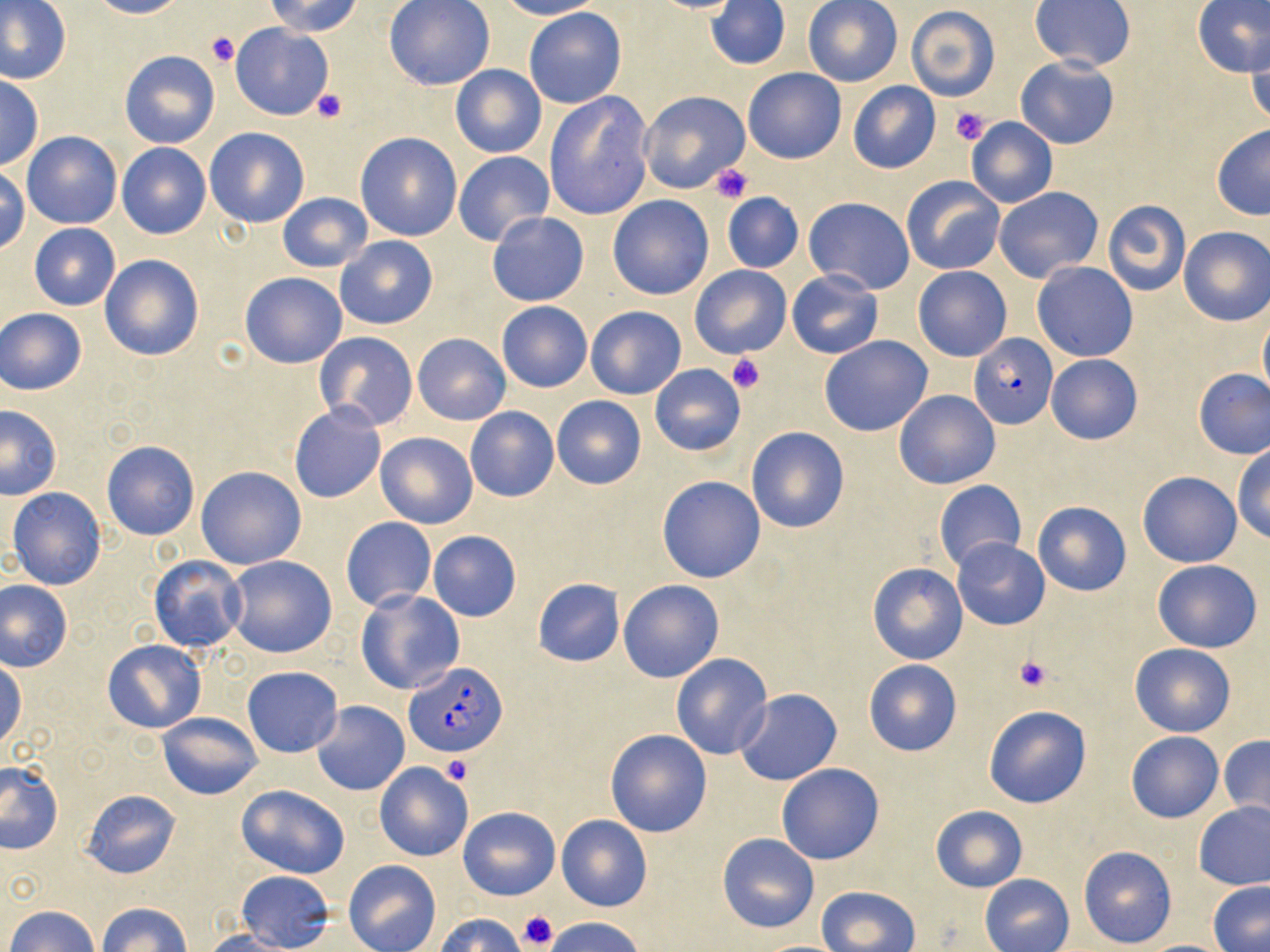

slide-level diagnosis = Plasmodium falciparum
field of view = one of a larger specimen
platelet locations = approximate bounding boxes as (x1, y1, x2, y2) in pixels: (206, 30, 241, 67), (312, 89, 346, 123), (952, 107, 992, 146), (710, 163, 754, 204), (727, 353, 765, 393), (1013, 655, 1054, 692), (440, 756, 472, 785), (516, 911, 557, 950)
magnification = 1000x
Plasmodium falciparum-infected red blood cell locations = approximate bounding boxes as (x1, y1, x2, y2) in pixels: (968, 335, 1058, 429), (404, 660, 506, 758)
preparation = thin blood smear
uninfected red blood cell locations = approximate bounding boxes as (x1, y1, x2, y2) in pixels: (86, 0, 186, 19), (266, 0, 362, 37), (383, 0, 494, 90), (494, 0, 603, 20), (644, 0, 746, 14), (1192, 0, 1268, 76), (706, 1, 790, 70), (803, 1, 903, 86), (1030, 1, 1135, 71), (0, 2, 70, 84), (906, 4, 1001, 102), (523, 7, 627, 109), (229, 22, 336, 121), (1245, 30, 1269, 127), (120, 50, 219, 149), (1015, 56, 1120, 149), (450, 64, 547, 158), (742, 67, 847, 164), (0, 74, 43, 171), (849, 82, 940, 173), (637, 89, 749, 194), (543, 90, 655, 220), (965, 115, 1058, 209), (1211, 124, 1270, 220), (205, 127, 310, 228), (22, 131, 121, 229), (354, 132, 462, 241), (117, 143, 212, 240), (453, 150, 555, 248), (1, 166, 29, 255), (900, 176, 1005, 276), (993, 186, 1104, 284), (277, 192, 372, 273), (722, 193, 803, 273), (607, 194, 714, 299), (804, 197, 915, 295), (1103, 200, 1190, 296), (486, 210, 590, 306), (30, 223, 121, 311), (1178, 226, 1270, 327), (335, 235, 438, 329), (100, 254, 204, 362), (1032, 261, 1138, 361), (690, 264, 791, 359), (913, 266, 1011, 361), (787, 271, 883, 359), (240, 272, 347, 369), (497, 302, 592, 392), (585, 305, 686, 400), (0, 308, 88, 395), (1259, 309, 1270, 404), (314, 331, 419, 431), (412, 334, 510, 425), (820, 336, 933, 436), (1047, 354, 1143, 445), (649, 364, 746, 455), (1193, 368, 1270, 459), (894, 389, 1000, 489), (551, 396, 647, 490), (289, 404, 386, 504), (0, 406, 62, 500), (465, 407, 559, 502), (746, 427, 849, 534), (375, 431, 477, 528), (101, 440, 200, 540), (1231, 445, 1270, 544), (195, 466, 306, 570), (1137, 471, 1242, 567), (658, 476, 765, 583), (933, 480, 1025, 573), (8, 487, 107, 591), (1033, 500, 1131, 596), (341, 517, 436, 611), (427, 530, 521, 621), (952, 538, 1049, 630), (224, 554, 337, 659), (149, 557, 247, 652), (1153, 558, 1261, 653), (867, 562, 968, 665), (533, 578, 624, 667), (618, 579, 724, 683), (1, 581, 72, 671), (355, 589, 464, 695), (102, 639, 205, 733), (1130, 642, 1236, 736), (671, 653, 773, 759), (0, 658, 24, 752), (863, 658, 962, 757), (242, 667, 343, 757), (734, 688, 842, 786), (311, 701, 409, 795), (983, 705, 1091, 808), (157, 713, 263, 800), (605, 729, 712, 838), (1125, 732, 1223, 823), (1219, 734, 1270, 827), (373, 762, 473, 862), (0, 763, 63, 854), (776, 763, 884, 865), (236, 783, 350, 879), (83, 789, 181, 880), (1193, 801, 1270, 890), (930, 805, 1026, 893), (458, 806, 560, 900), (556, 813, 652, 911), (718, 833, 819, 933), (1078, 846, 1178, 949), (343, 860, 441, 952), (239, 872, 337, 951), (981, 875, 1074, 952), (1208, 883, 1270, 951), (815, 885, 921, 951), (96, 902, 193, 952), (6, 906, 99, 952), (436, 913, 527, 952), (544, 916, 646, 952), (201, 931, 296, 952)
image size = 1270×952 pixels
modality = optical microscopy
stain = May-Grünwald-Giemsa